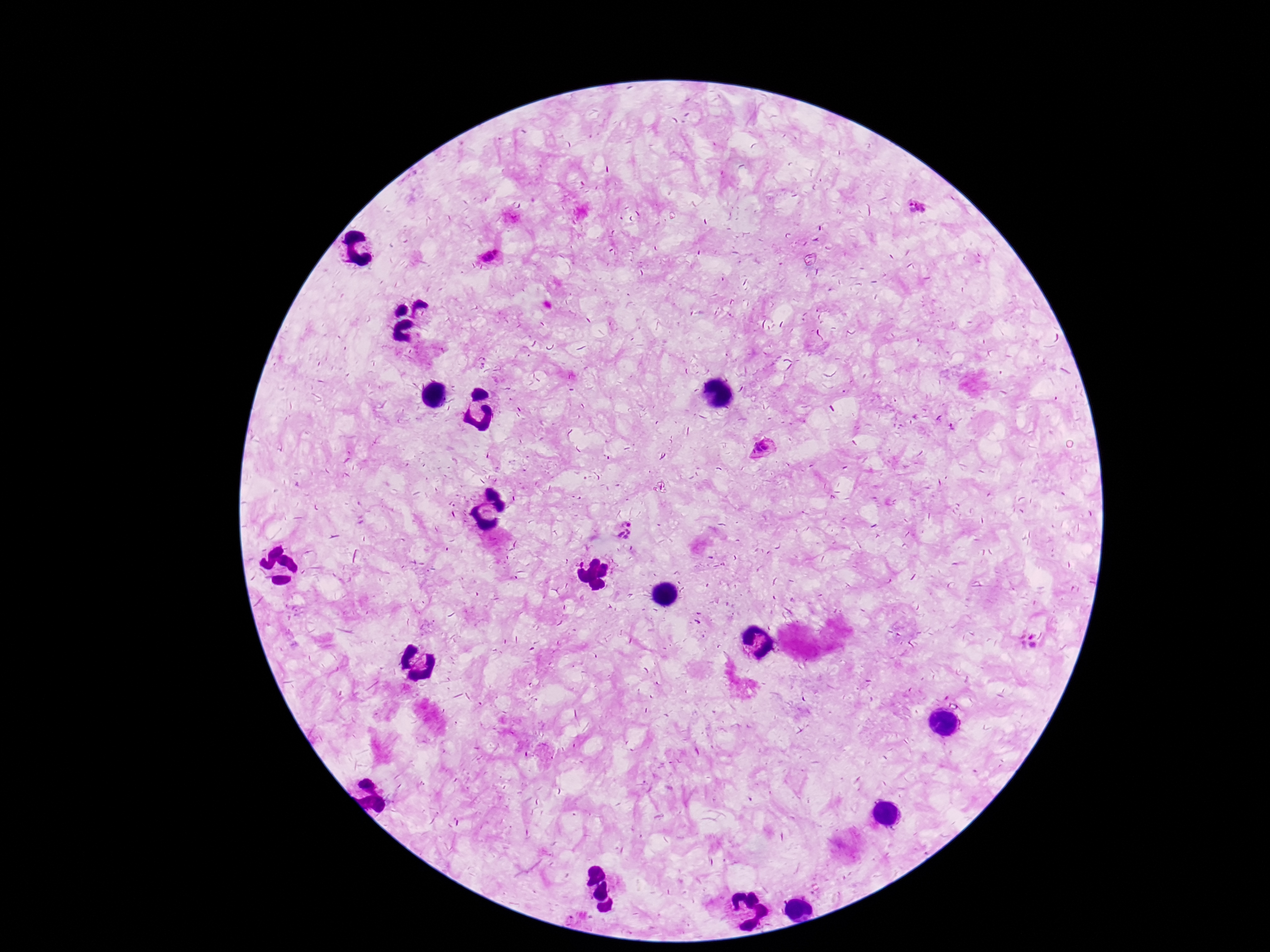

field_of_view: one from this slide
magnification: 100x
patient_malaria_status: infected
preparation: thick blood film
stain: Giemsa
image_size: 1270×952 pixels
capture: smartphone camera through the microscope eyepiece
plasmodium_parasite_locations: 'approximate centers as [x, y] in pixels: [918, 207], [495, 251], [487, 257], [763, 448], [625, 529], [1028, 640]'